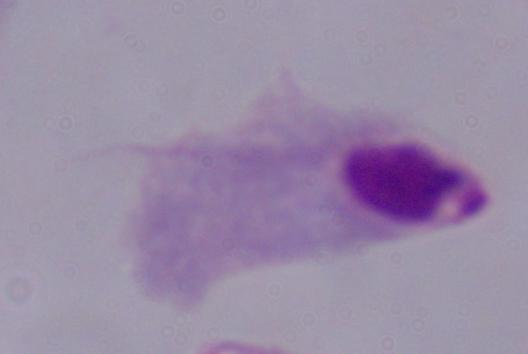

Summary:
  - Modality: photomicrograph
  - Magnification: 1000x
  - Identification: trichomonad